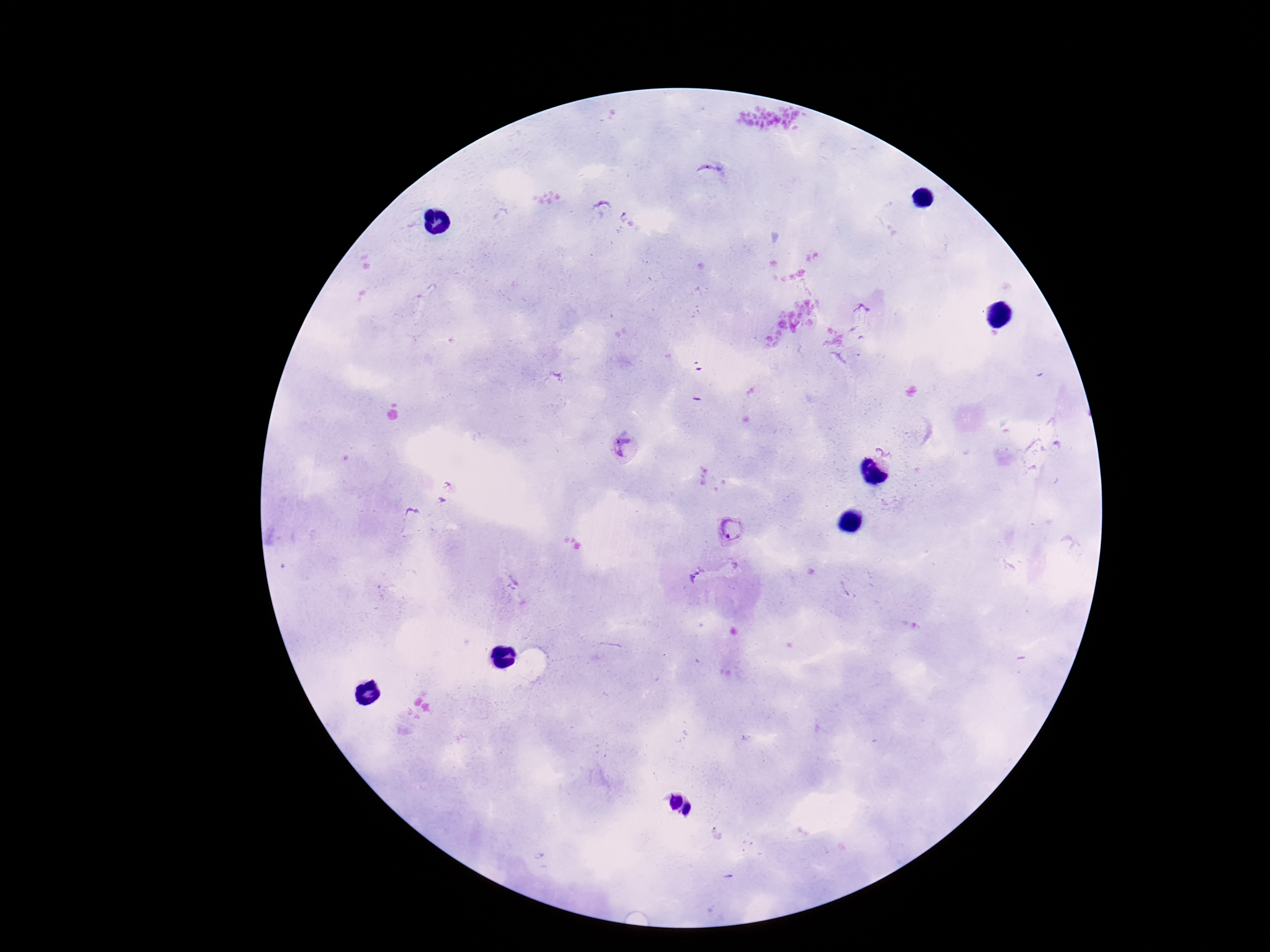
Approximate centers as (x, y) in pixels.
Summary:
  - Plasmodium parasite locations: (623, 447), (729, 529)
  - Capture: smartphone camera through the microscope eyepiece
  - Magnification: 100x
  - Image size: 1270×952 pixels
  - Preparation: thick peripheral-blood smear
  - Patient malaria status: positive
  - Stain: Giemsa
  - Field of view: one from this slide